Report the malaria status of this cell.
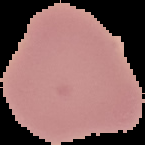

Uninfected.

image type = cell region segmented out of the field of view; surrounding area masked to black
preparation = thin blood smear
image size = 145×145 pixels